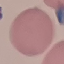
Summary:
  - Result: no malaria parasites detected
  - Preparation: thin blood smear
  - Image type: cell patch, automatically extracted from a larger field of view and resized to 64 × 64 pixels
  - Stain: Giemsa
  - Capture: smartphone camera at the microscope eyepiece